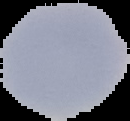 From a thin blood smear. Malaria status: uninfected. Image is 130×121 pixels. Segmented cell region on a black background.